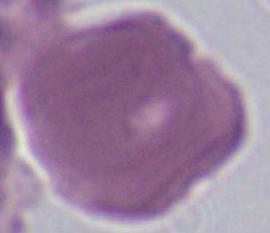

identification: erythrocyte
magnification: 1000x
modality: photomicrograph